Evaluate for parasitized red blood cells.
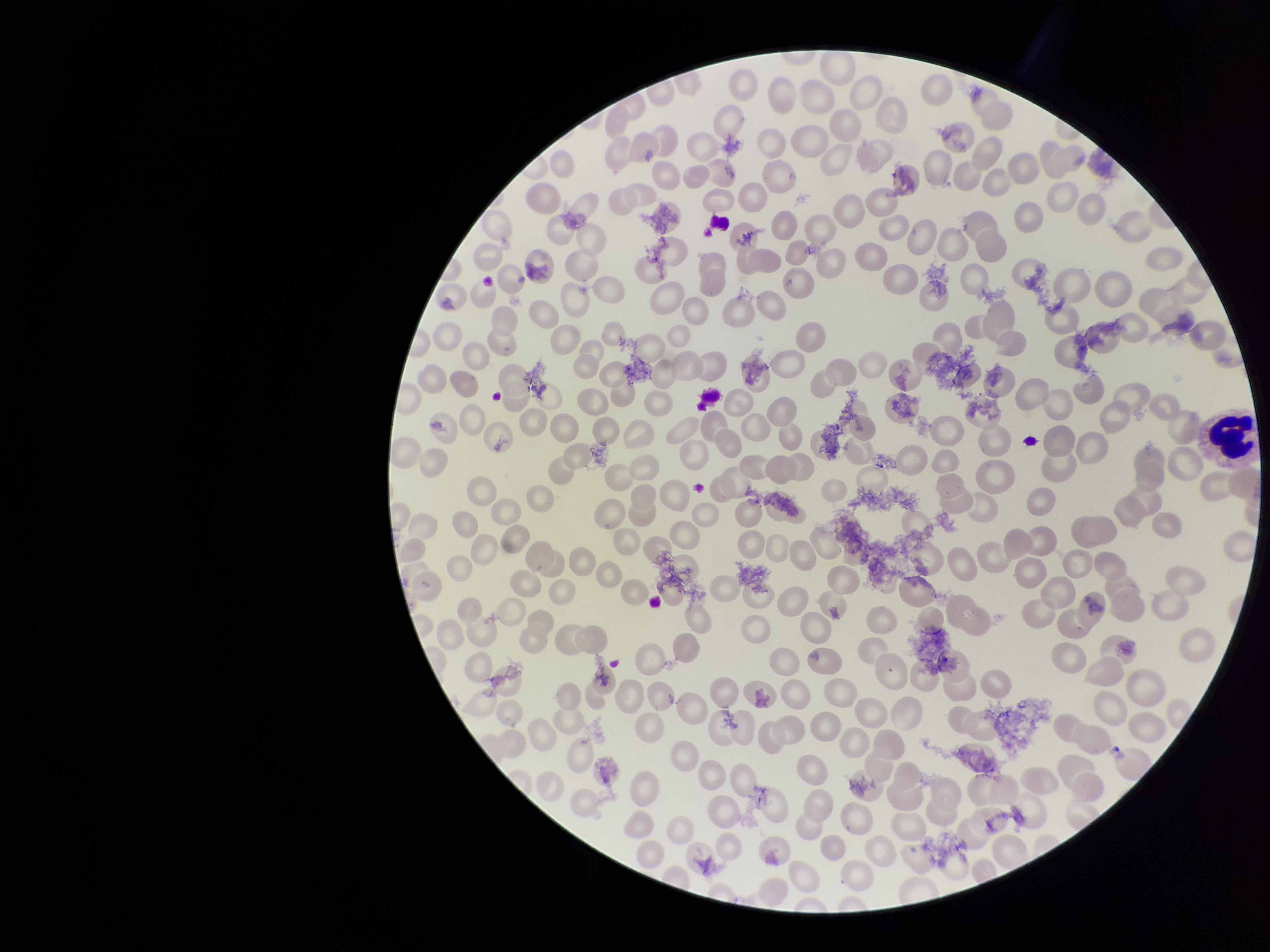

None seen.

red_blood_cell_count: 215
patient_malaria_status: negative
capture: smartphone photograph through the microscope eyepiece
preparation: thin
image_size: 1270×952 pixels
field_of_view: single
parasitized_red_blood_cell_count: 0
stain: Giemsa